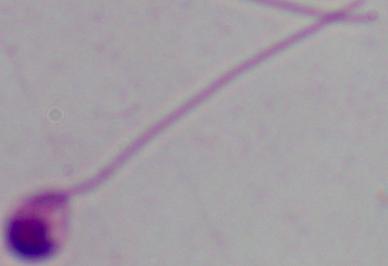
Photomicrograph. 1000x magnification. A Leishmania parasite is shown.